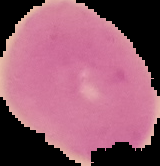

{
  "image_type": "cell region segmented out of the field of view; surrounding area masked to black",
  "image_size": "160×166 pixels",
  "preparation": "thin blood smear",
  "malaria_status": "uninfected"
}